Comment on the morphology of the red blood cells.
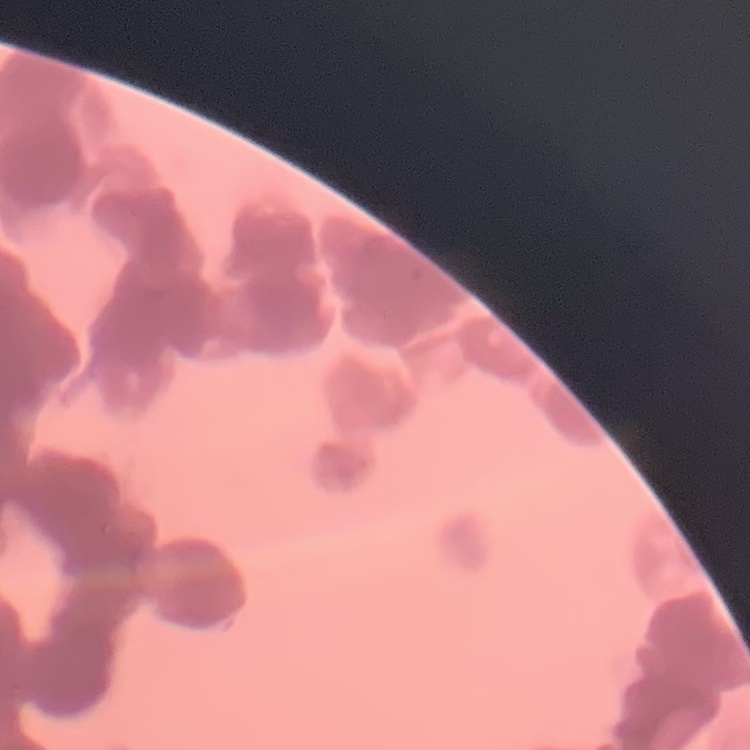
Rouleaux formation.

image type = one tile cut from a larger photomicrograph
preparation = thin peripheral smear
stain = Field's or Giemsa